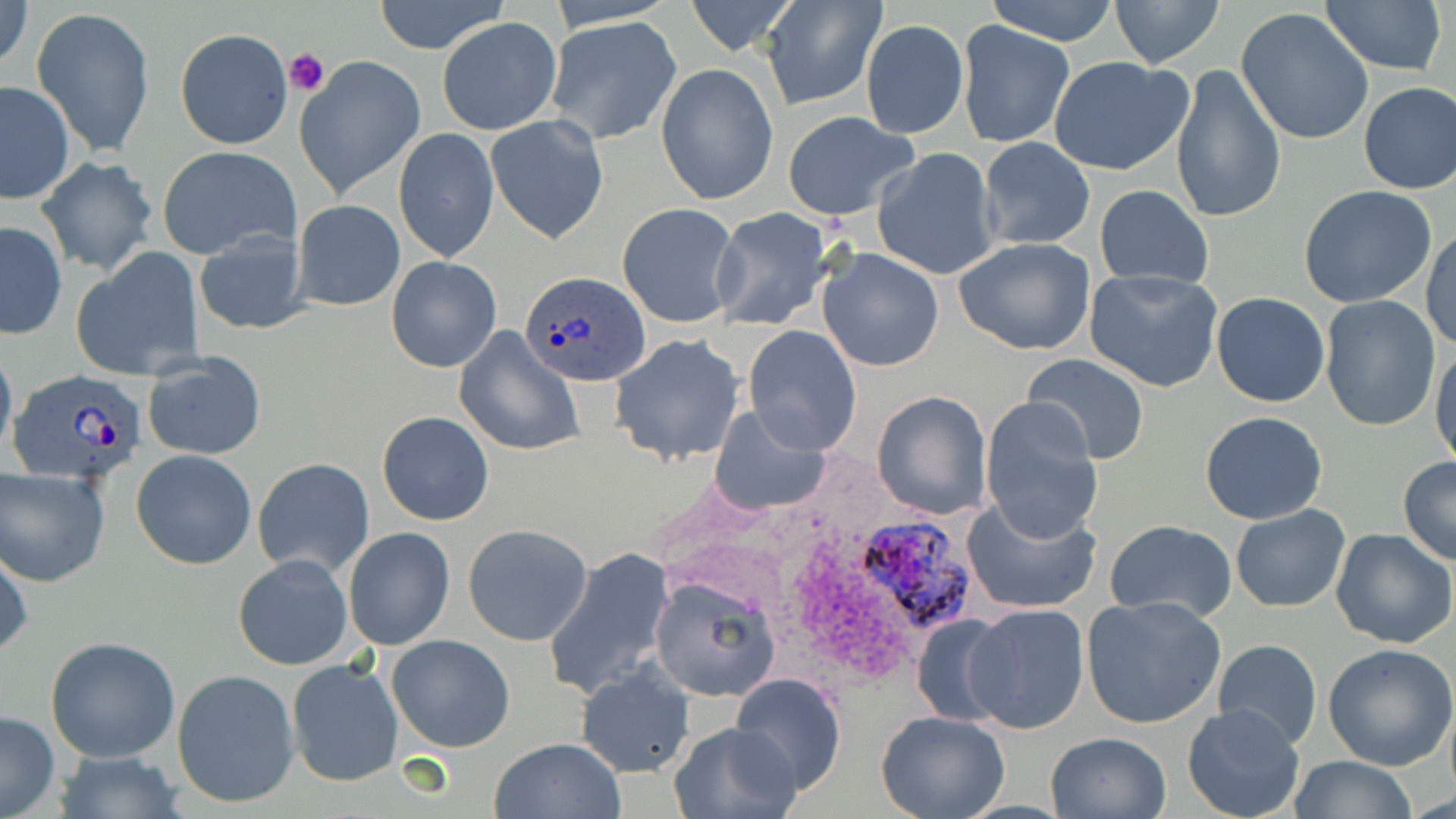

Approximate bounding boxes as (x1,y1)-(x2,y2) corner pairs in pixels. Platelet locations: (282,48)-(329,96). Uninfected red blood cell locations: (1,0)-(33,74), (374,0)-(511,55), (543,0)-(681,30), (682,0)-(800,55), (760,0)-(888,111), (982,0)-(1121,45), (1110,0)-(1225,69), (1319,0)-(1447,74), (31,6)-(155,158), (1235,8)-(1375,146), (544,16)-(682,145), (437,17)-(562,135), (861,19)-(968,139), (957,22)-(1074,148), (175,29)-(292,149), (294,56)-(426,199), (1048,56)-(1193,176), (655,64)-(780,204), (1170,65)-(1287,226), (0,80)-(76,205), (1357,81)-(1455,195), (781,111)-(919,221), (485,115)-(610,246), (393,129)-(499,262), (976,137)-(1095,250), (156,145)-(300,260), (872,147)-(1002,281), (36,157)-(160,276), (1299,184)-(1438,309), (1094,185)-(1214,289), (292,199)-(405,311), (618,202)-(741,329), (708,206)-(839,331), (0,221)-(68,340), (1422,228)-(1456,352), (192,230)-(309,335), (953,236)-(1097,356), (70,248)-(204,382), (816,248)-(946,372), (386,258)-(502,372), (1085,270)-(1224,392), (1210,293)-(1330,408), (1318,296)-(1440,432), (742,326)-(863,454), (454,327)-(584,455), (610,335)-(747,465), (0,341)-(18,465), (1431,344)-(1454,474), (142,354)-(268,460), (1023,354)-(1150,466), (873,389)-(993,520), (979,397)-(1105,543), (708,406)-(832,513), (376,411)-(495,526), (1201,411)-(1328,525), (131,450)-(257,569), (253,457)-(375,579), (1398,457)-(1455,565), (0,467)-(114,586), (962,493)-(1101,614), (1230,504)-(1351,612), (1106,520)-(1238,622), (463,524)-(593,646), (343,526)-(455,650), (1330,528)-(1455,647), (0,541)-(33,660), (544,547)-(676,700), (234,554)-(352,670), (649,576)-(779,703), (1081,595)-(1227,729), (963,602)-(1090,736), (911,611)-(1022,725), (45,636)-(180,762), (386,636)-(515,753), (1212,640)-(1323,750), (1324,643)-(1456,772), (287,659)-(403,787), (575,664)-(694,777), (172,668)-(300,808), (732,674)-(846,798), (1182,704)-(1306,819), (0,709)-(61,819), (875,710)-(1009,819), (669,719)-(805,818), (1046,731)-(1171,818), (489,737)-(626,819), (54,749)-(184,817), (1288,756)-(1419,817). Plasmodium ovale-infected red blood cell locations: (516,269)-(654,386), (12,367)-(154,483), (860,517)-(979,631). Slide-level diagnosis: Plasmodium ovale. Optical microscopy. Single field of view. Image is 1456×819 pixels. Thin blood smear. May-Grünwald-Giemsa-stained preparation. 1000x magnification.